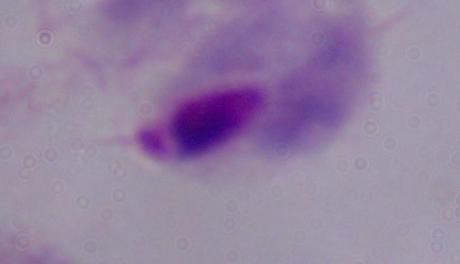 Captured at 1000x magnification. Photomicrograph. A trichomonad is shown.